Name the parasite shown.
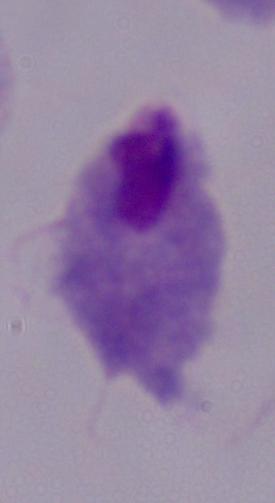

A trichomonad.

modality: micrograph
magnification: 1000x